Give the preparation type.
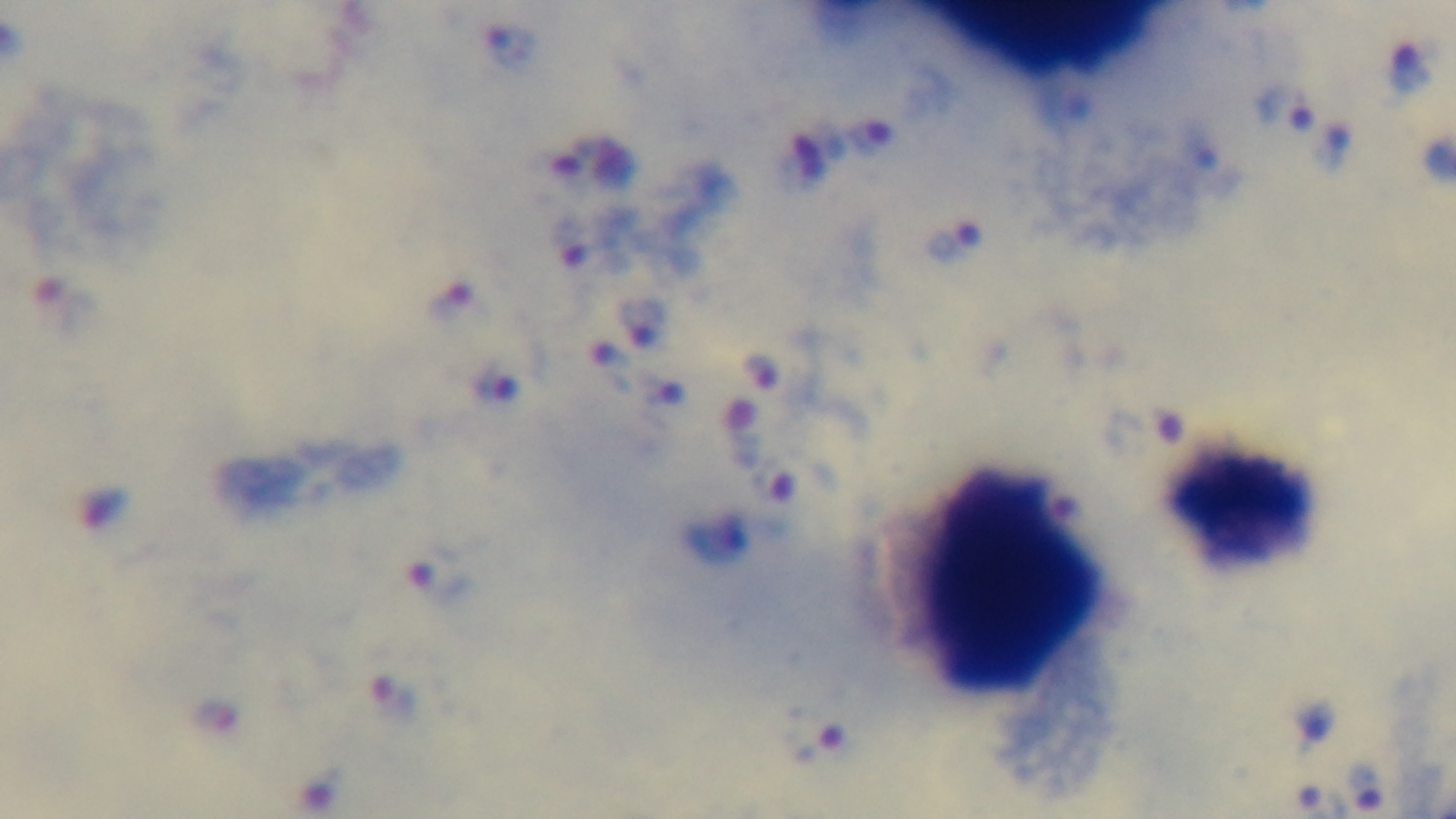
It is a thick blood film.

stain = Giemsa
capture = mounted 4K digital camera
malaria status = positive
objective = 100x oil immersion
field of view = single
modality = light microscopy